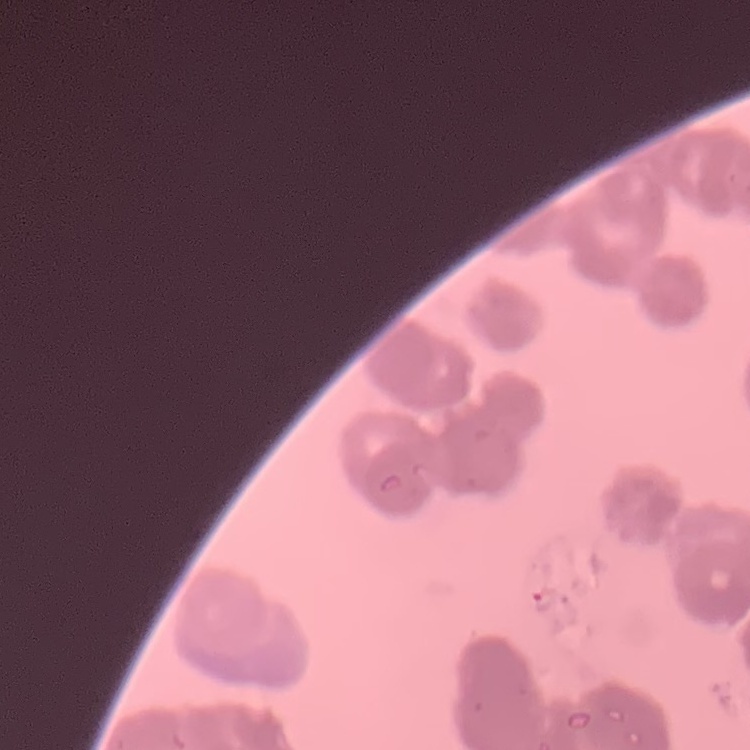 The erythrocytes exhibit rouleaux formation. One tile cut from a larger photomicrograph. Stained with either Field's or Giemsa. Thin blood smear.